Give the preparation type.
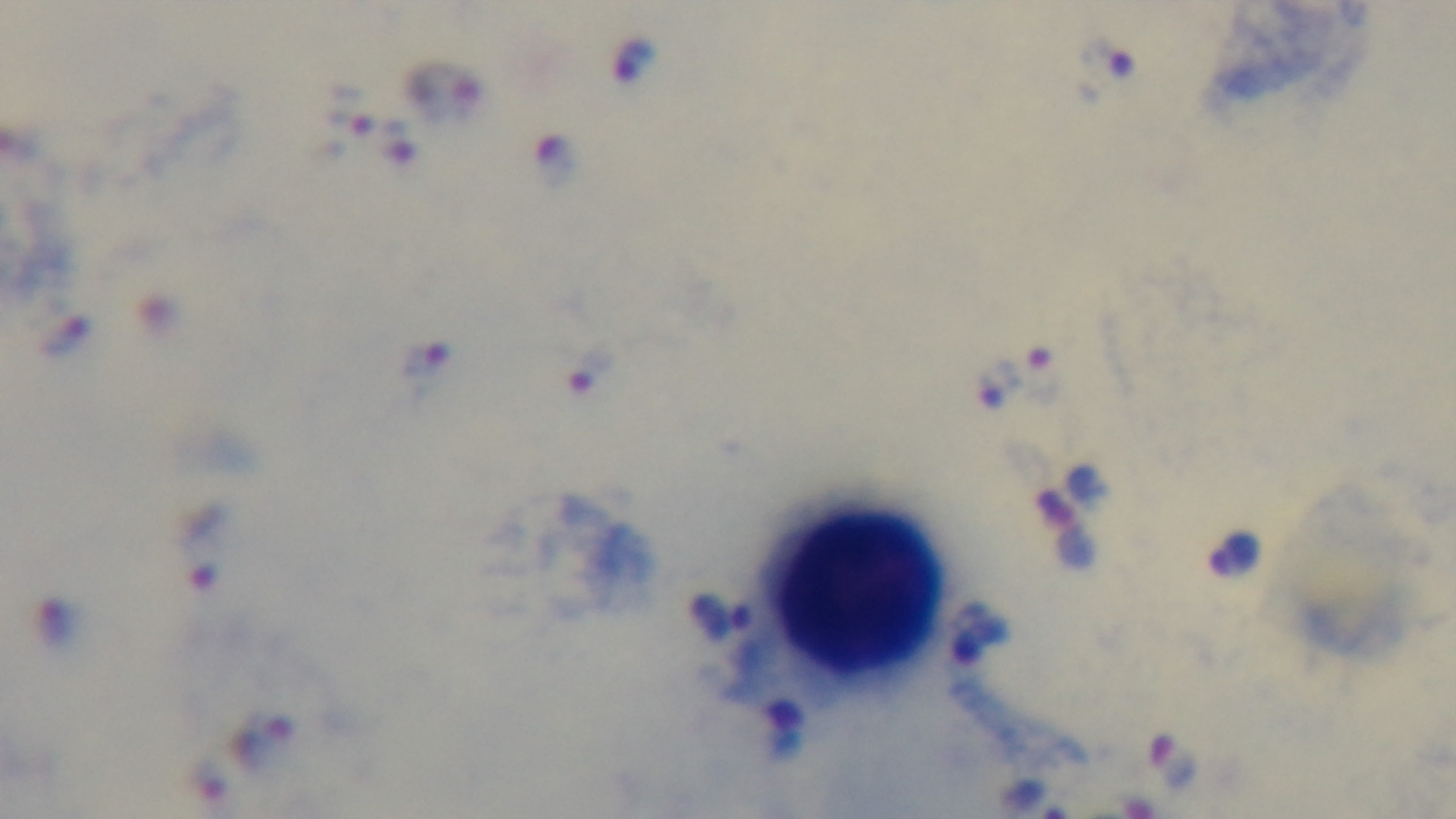
It is a thick blood film.

Summary:
  - Capture: mounted 4K digital camera
  - Modality: light microscopy
  - Objective: 100x oil immersion
  - Stain: Giemsa
  - Malaria status: infected
  - Field of view: one from the slide